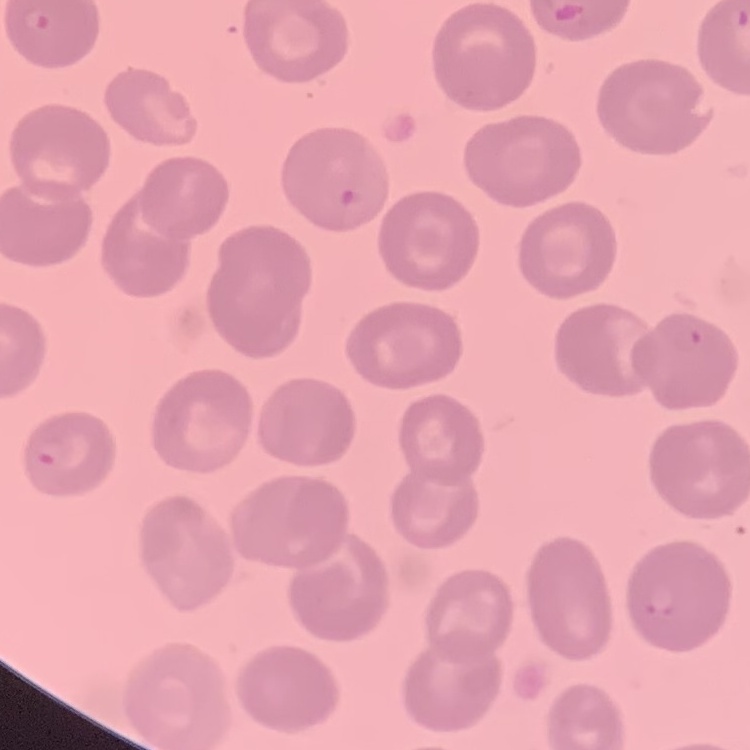

The red blood cells exhibit no rouleaux formation. Stained with either Field's or Giemsa. One tile cut from a larger photomicrograph. Thin blood film.